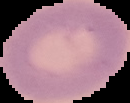 From a thin blood smear. Cell region segmented out of the field of view; the surrounding area is masked to black. Image is 130×103 pixels. Result: no Plasmodium parasites detected.